Assess the morphology of the erythrocytes.
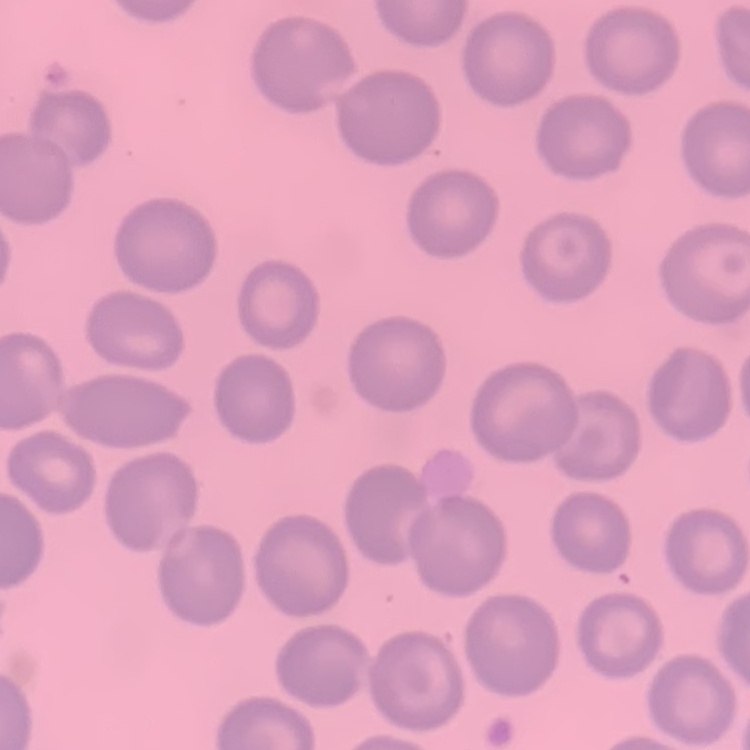
They show no rouleaux formation.

{
  "preparation": "thin blood film",
  "stain": "Field's or Giemsa",
  "image_type": "one tile cut from a larger photomicrograph"
}